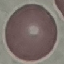
result = no malaria parasites seen
capture = smartphone through the microscope eyepiece
preparation = thin blood smear
stain = Giemsa
image type = automatically extracted cell patch, resized to 64 × 64 pixels